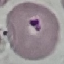
malaria status = uninfected
preparation = thin blood smear
capture = smartphone camera at the microscope eyepiece
stain = Giemsa
image type = automatically extracted cell patch, resized to 64 × 64 pixels